Classify this cell by malaria status.
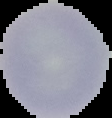
It is uninfected.

Image is 112×118 pixels. From a thin blood smear. Segmented cell region on a black background.